Give the position of every leukocyte visible.
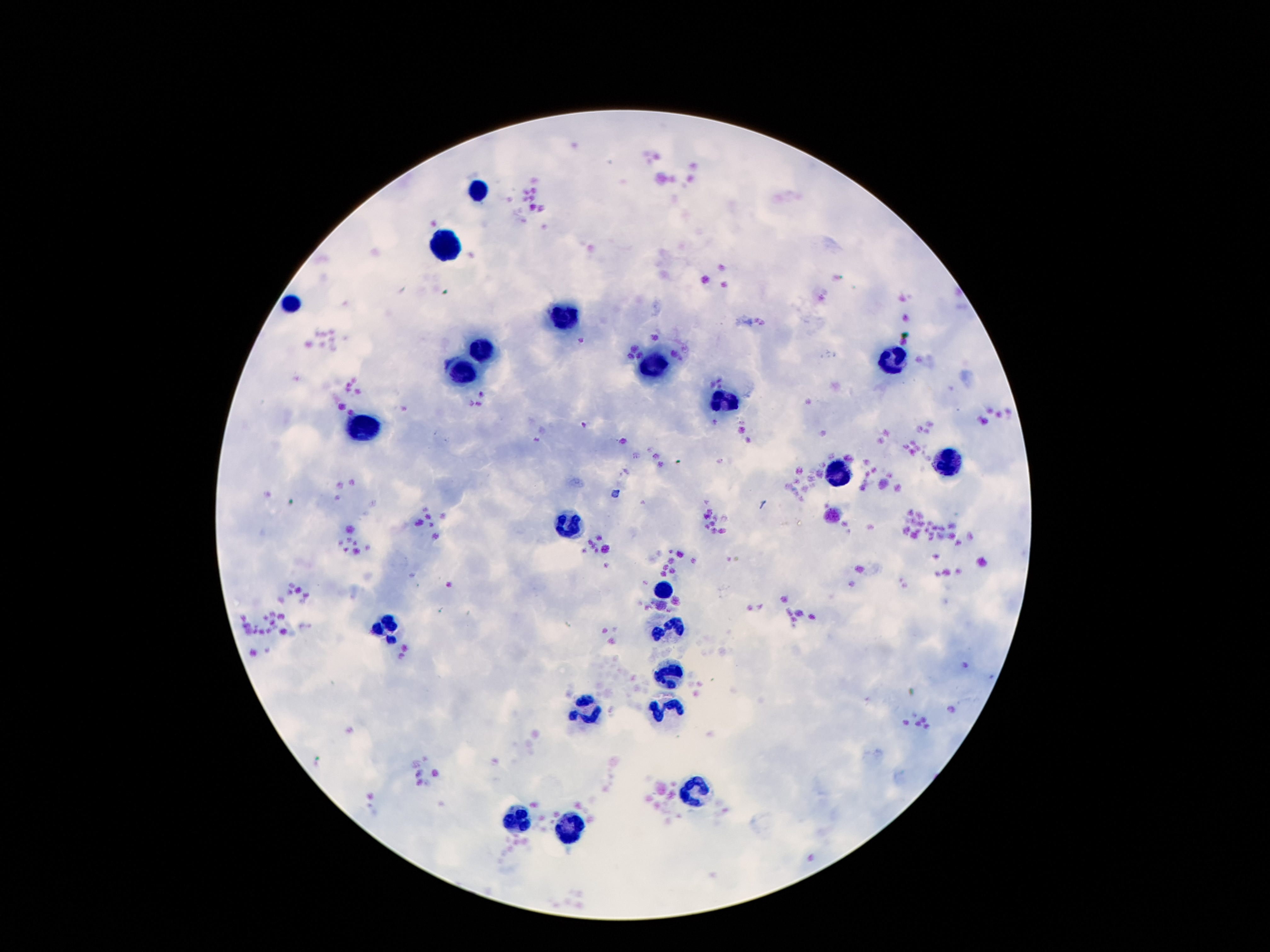

Approximate object centers, in pixels from the top-left corner.
Leukocytes: (x=477, y=187), (x=447, y=250), (x=290, y=302), (x=567, y=320), (x=481, y=347), (x=892, y=359), (x=651, y=367), (x=458, y=369), (x=722, y=404), (x=365, y=431), (x=945, y=462), (x=840, y=471), (x=571, y=523), (x=664, y=588), (x=384, y=625), (x=668, y=631), (x=670, y=671), (x=664, y=711), (x=584, y=713), (x=693, y=795), (x=517, y=822), (x=569, y=828).

Photographed through the microscope eyepiece with a smartphone camera. Thick blood smear. Patient malaria status: not infected. 100x magnification. Giemsa-stained preparation. Image is 1270×952 pixels. Single field of view.